Report the malaria status of this cell.
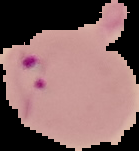
It is parasitized.

Summary:
  - Image size: 139×151 pixels
  - Image type: segmented cell region with the area outside set to black
  - Preparation: thin blood smear